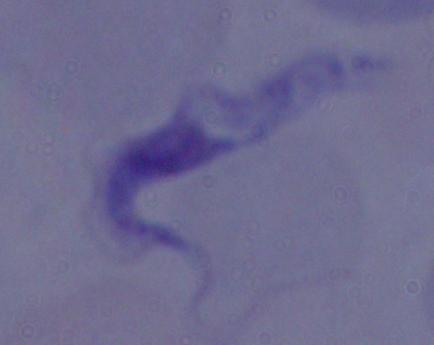

modality: photomicrograph
identification: trypanosome
magnification: 1000x